Give the preparation type.
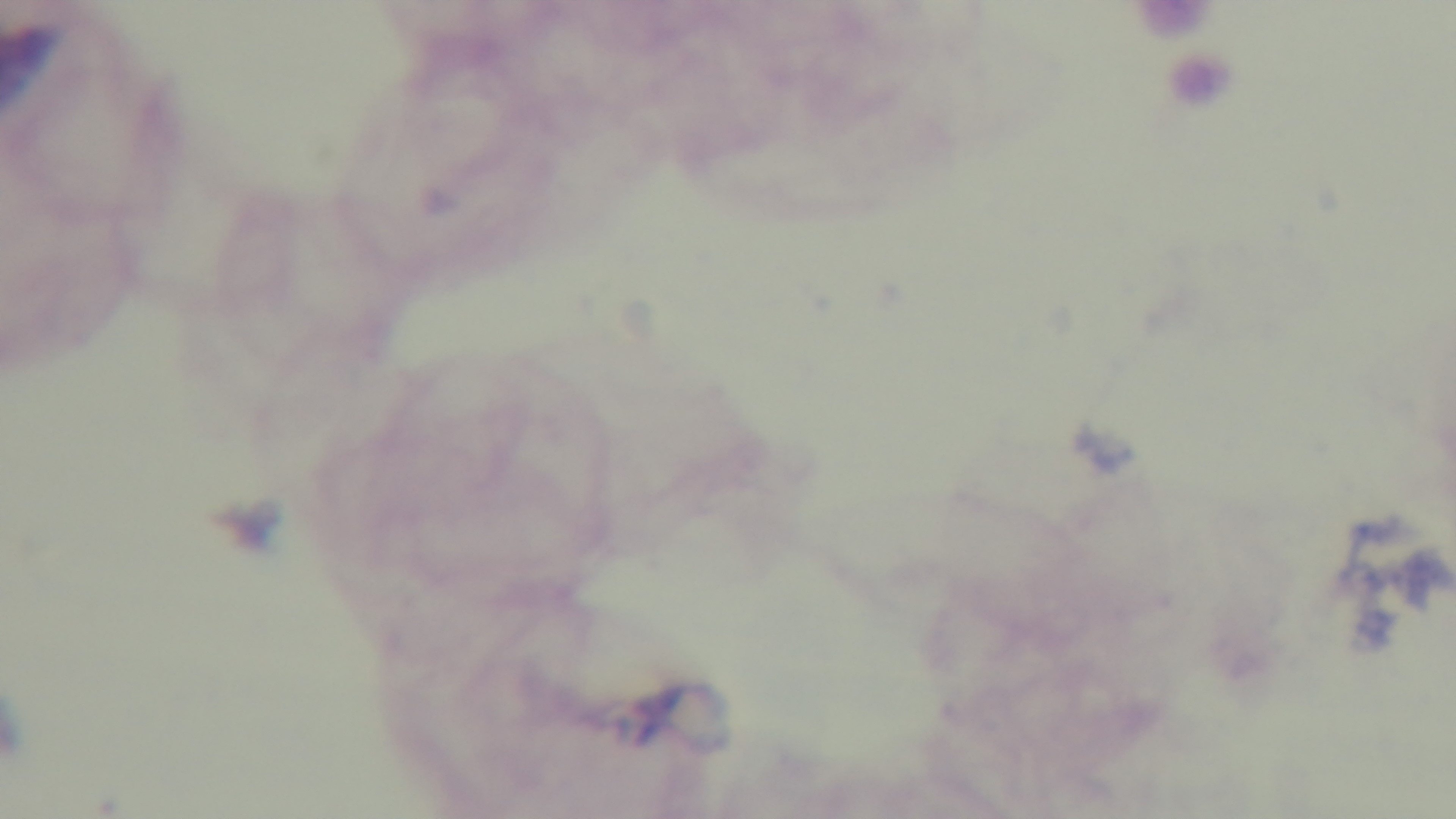

A thick smear.

Giemsa stain. Single field of view. Light microscopy. Mounted 4K digital camera. Malaria status: uninfected. 100x oil-immersion objective.